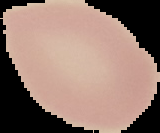

Summary:
  - Malaria status: uninfected
  - Image type: segmented cell region with the area outside set to black
  - Image size: 160×133 pixels
  - Preparation: thin blood film